Assess this cell for malaria.
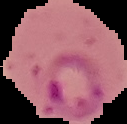

It is parasitized.

image type = cell region segmented out of the field of view; surrounding area masked to black
image size = 127×124 pixels
preparation = thin blood smear